Assess the morphology of the erythrocytes.
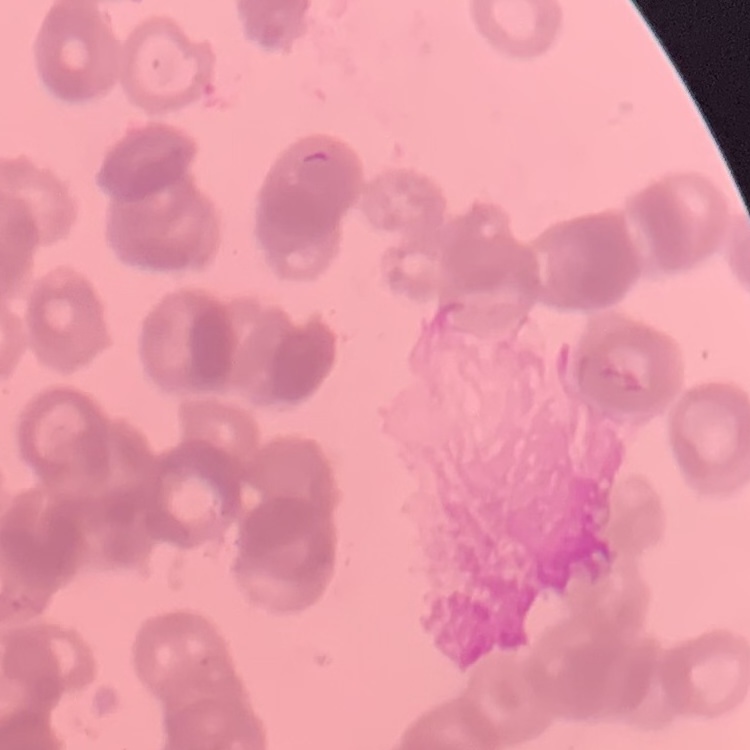
They show rouleaux formation.

{
  "stain": "Field's or Giemsa",
  "image_type": "square crop of a larger photomicrograph",
  "preparation": "thin blood film"
}